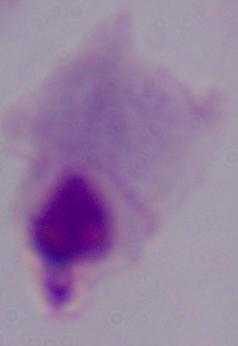
Summary:
  - Modality: micrograph
  - Magnification: 1000x
  - Identification: trichomonad